Outline each Plasmodium parasite.
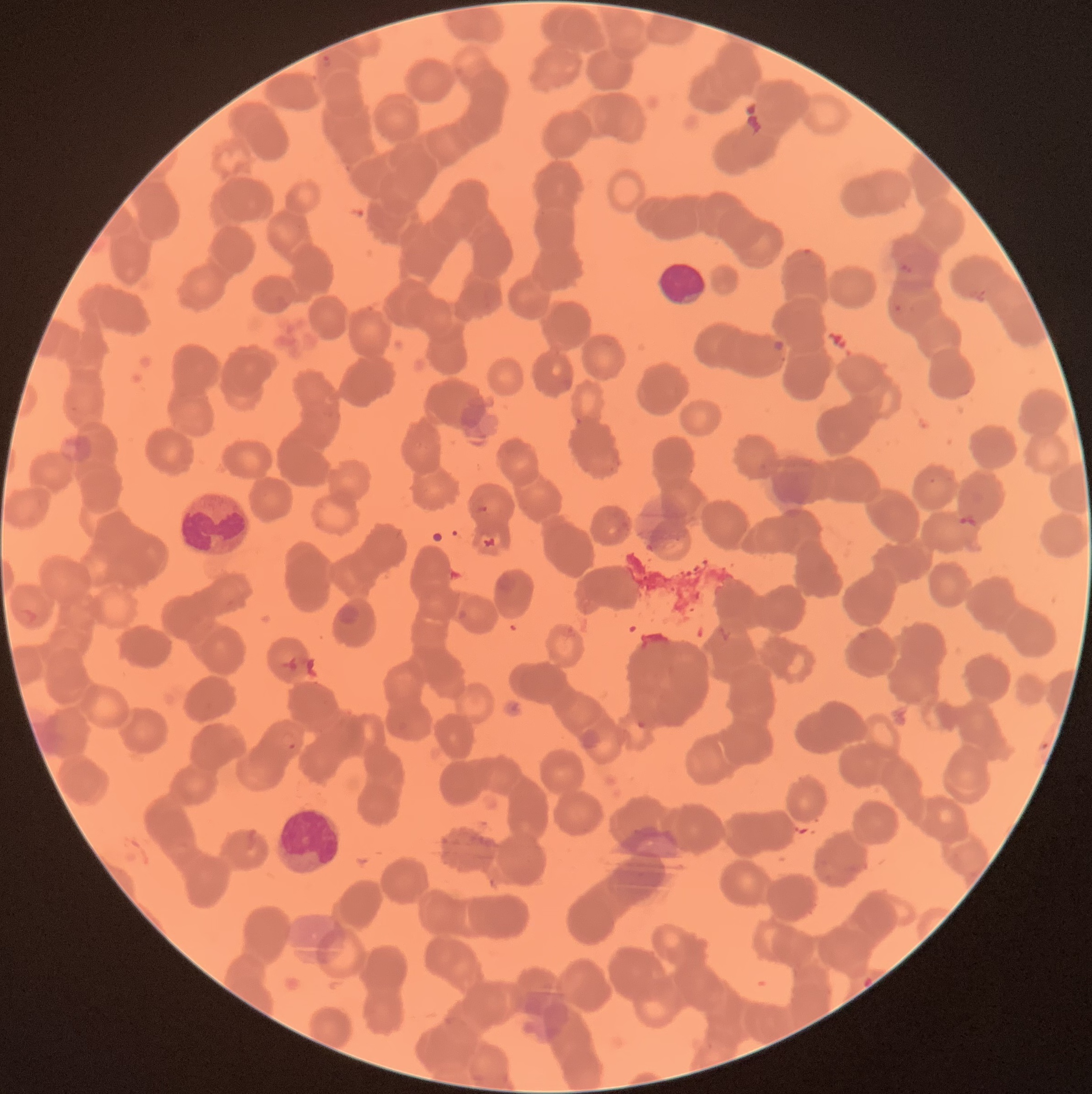
Approximate bounding boxes as (x1, y1, x2, y2) in pixels.
Plasmodium parasites: (320, 55, 333, 70), (900, 263, 913, 274), (893, 303, 904, 314), (770, 339, 785, 355), (473, 504, 488, 514), (959, 513, 978, 530), (636, 719, 648, 731), (279, 733, 297, 750), (863, 976, 873, 988).

Summary:
  - White blood cell locations: (658, 262, 707, 308), (180, 492, 249, 557), (273, 803, 343, 876)
  - Modality: optical microscopy
  - Red blood cell morphology: rouleaux formation
  - Image size: 1092×1094 pixels
  - Preparation: thin blood smear